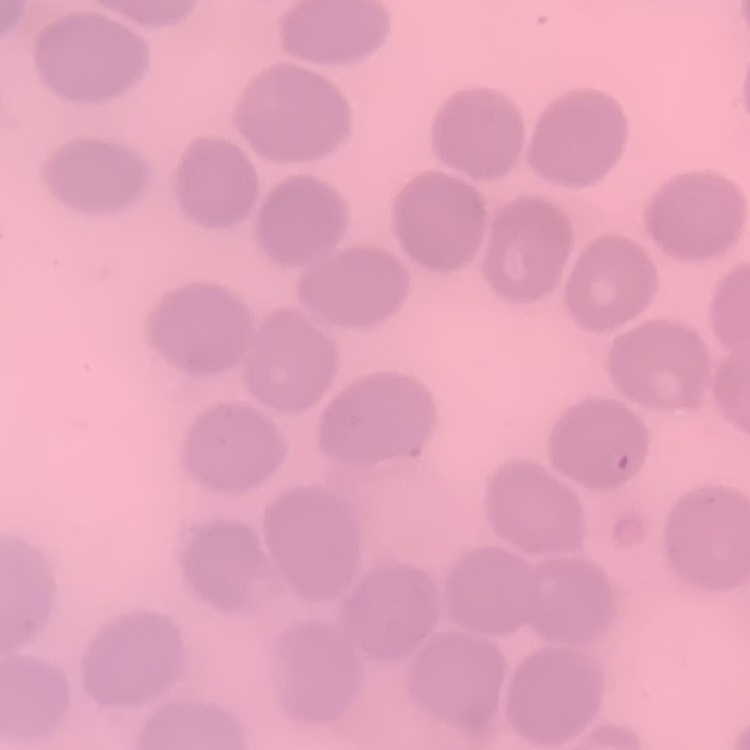

red blood cell morphology = no rouleaux formation
image type = one tile cut from a larger photomicrograph
stain = Field's or Giemsa
preparation = thin peripheral smear